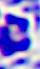
Summary:
  - Magnification: 400x
  - Identification: white blood cell
  - Modality: photomicrograph